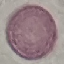

malaria status = uninfected
stain = Giemsa
image type = automatically extracted cell patch, resized to 64 × 64 pixels
preparation = thin blood film
capture = smartphone camera at the microscope eyepiece